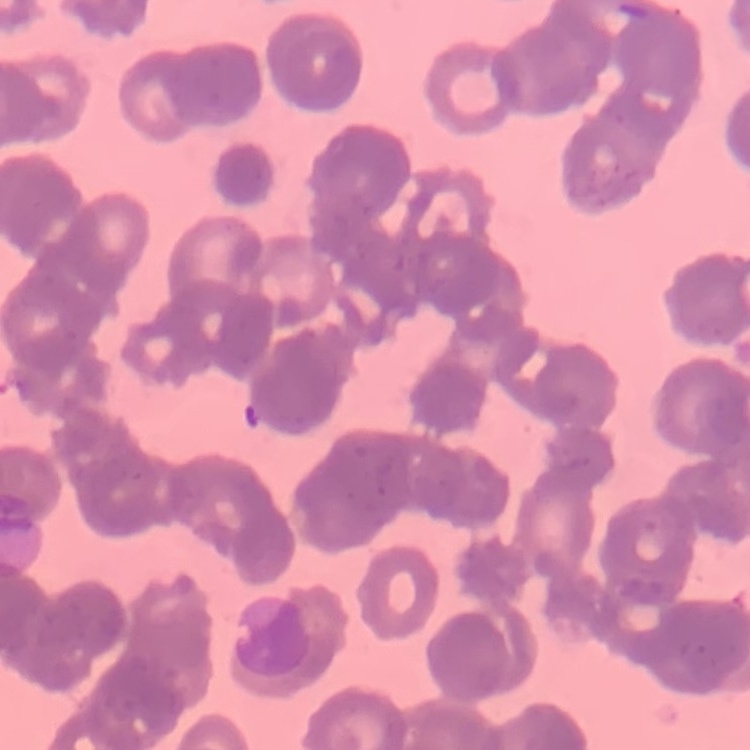 The erythrocytes show rouleaux formation. Thin blood smear. Field's or Giemsa stain. One tile cut from a larger photomicrograph.